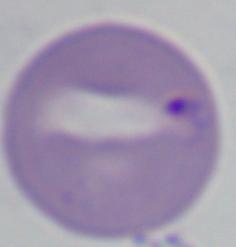

modality = micrograph
identification = Babesia
magnification = 1000x